Locate every Plasmodium malariae-infected red blood cell.
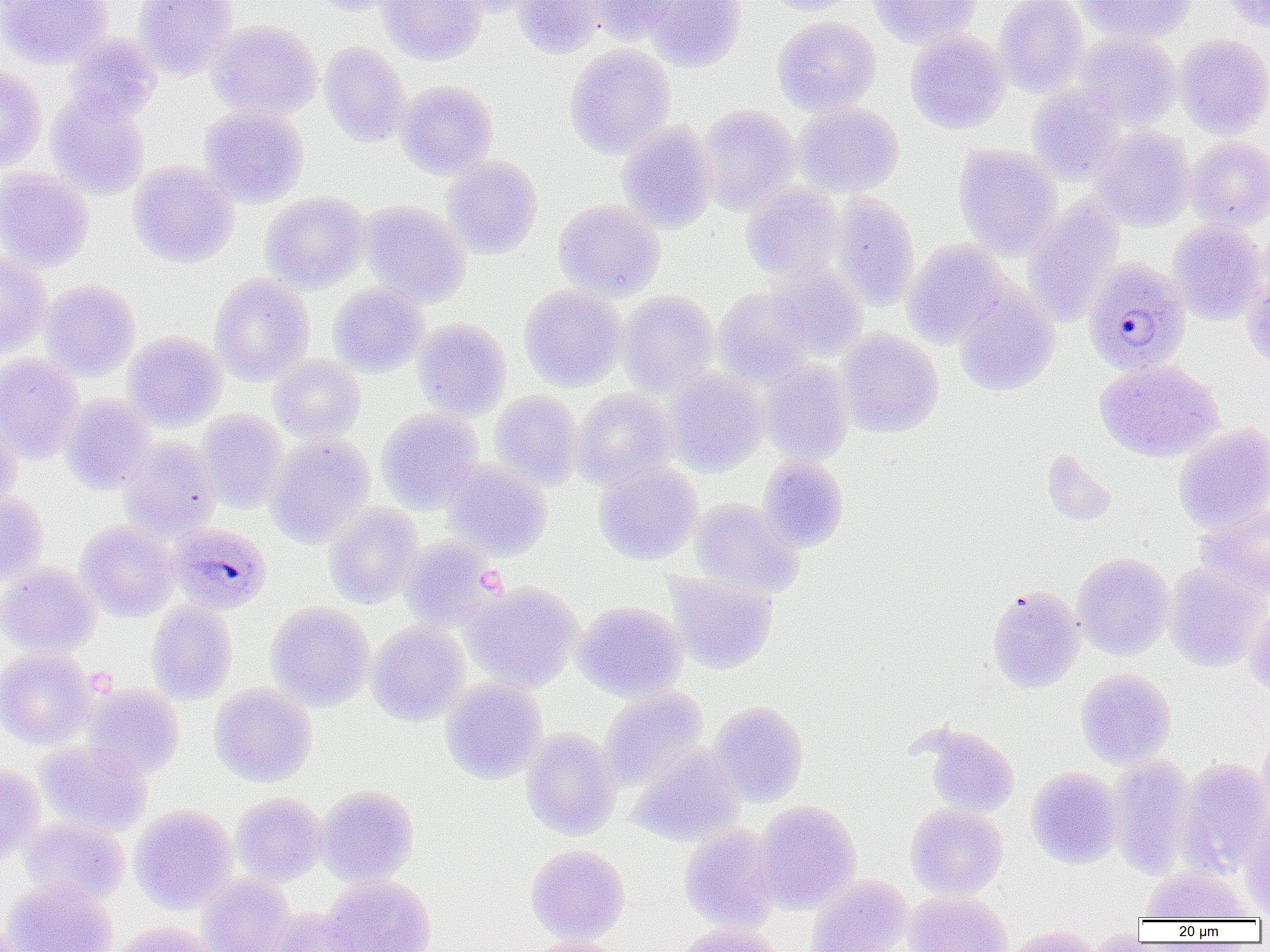

Approximate bounding boxes as (x1, y1, x2, y2) in pixels.
Plasmodium malariae-infected red blood cells: (1092, 257, 1199, 375), (168, 522, 272, 614).

Summary:
  - Uninfected red blood cell locations: (0, 0, 113, 69), (132, 0, 238, 79), (309, 0, 406, 16), (379, 0, 487, 65), (449, 0, 546, 16), (514, 0, 604, 58), (590, 0, 682, 45), (647, 0, 746, 71), (764, 0, 862, 15), (868, 0, 981, 48), (995, 0, 1088, 96), (1076, 0, 1196, 44), (1221, 0, 1270, 33), (772, 16, 881, 115), (208, 19, 322, 120), (906, 29, 1009, 133), (1075, 31, 1180, 129), (63, 33, 162, 124), (1174, 34, 1270, 138), (319, 41, 410, 147), (565, 44, 675, 158), (0, 65, 47, 173), (396, 79, 498, 179), (1027, 86, 1124, 184), (46, 93, 150, 200), (794, 102, 904, 197), (698, 104, 800, 215), (200, 105, 309, 206), (618, 121, 717, 233), (1091, 126, 1195, 231), (1185, 136, 1270, 230), (953, 144, 1062, 259), (442, 156, 542, 259), (128, 160, 239, 268), (0, 167, 94, 271), (741, 181, 843, 281), (261, 191, 370, 292), (829, 191, 919, 310), (1023, 197, 1125, 326), (554, 199, 665, 300), (362, 201, 471, 307), (1169, 219, 1267, 324), (902, 240, 1009, 347), (0, 251, 52, 358), (767, 262, 867, 359), (1241, 270, 1270, 371), (210, 273, 314, 385), (41, 279, 140, 381), (328, 282, 427, 377), (954, 284, 1059, 396), (520, 285, 627, 391), (714, 287, 815, 386), (619, 291, 719, 396), (413, 318, 511, 420), (837, 329, 944, 437), (123, 331, 227, 431), (0, 353, 85, 462), (269, 354, 366, 442), (761, 359, 853, 463), (1095, 359, 1223, 462), (665, 369, 767, 476), (572, 388, 676, 489), (490, 390, 583, 490), (61, 394, 156, 494), (0, 408, 21, 511), (377, 408, 483, 512), (197, 410, 288, 513), (1173, 423, 1270, 533), (267, 434, 374, 547), (120, 437, 221, 541), (1041, 449, 1117, 526), (758, 455, 849, 551), (444, 459, 552, 560), (594, 460, 702, 564), (0, 488, 47, 584), (690, 498, 804, 597), (324, 503, 423, 609), (1196, 503, 1270, 601), (75, 520, 178, 621), (400, 536, 500, 629), (1072, 552, 1174, 660), (1164, 561, 1269, 672), (0, 562, 100, 656), (664, 571, 778, 674), (463, 581, 583, 692), (986, 584, 1084, 693), (146, 601, 237, 704), (266, 601, 374, 710), (573, 601, 686, 700), (1244, 603, 1270, 698), (368, 621, 470, 725), (0, 647, 96, 749), (1075, 668, 1176, 769), (441, 678, 546, 784), (81, 683, 184, 779), (210, 683, 316, 786), (600, 686, 708, 789), (708, 701, 808, 806), (921, 724, 1020, 817), (521, 728, 621, 840), (1258, 728, 1270, 820), (35, 739, 152, 837), (627, 745, 744, 847), (1107, 755, 1196, 880), (1177, 757, 1270, 875), (0, 765, 45, 864), (1025, 767, 1123, 869), (317, 784, 419, 886), (232, 792, 327, 885), (754, 800, 861, 913), (906, 803, 1007, 899), (130, 804, 237, 912), (1241, 804, 1269, 918), (19, 816, 129, 906), (679, 824, 780, 932), (526, 844, 630, 945), (1140, 864, 1253, 920), (198, 872, 295, 952), (806, 874, 913, 951), (323, 875, 436, 952), (2, 877, 117, 952), (904, 891, 1012, 952), (265, 906, 361, 951), (113, 921, 220, 952), (0, 922, 39, 952), (678, 922, 787, 952), (1000, 926, 1105, 952), (526, 936, 628, 952)
  - Slide-level diagnosis: Plasmodium malariae
  - Preparation: thin blood smear
  - Magnification: 1000x
  - Modality: optical microscopy
  - Field of view: one of a larger specimen
  - Image size: 1270×952 pixels